Locate every Plasmodium falciparum-infected red blood cell.
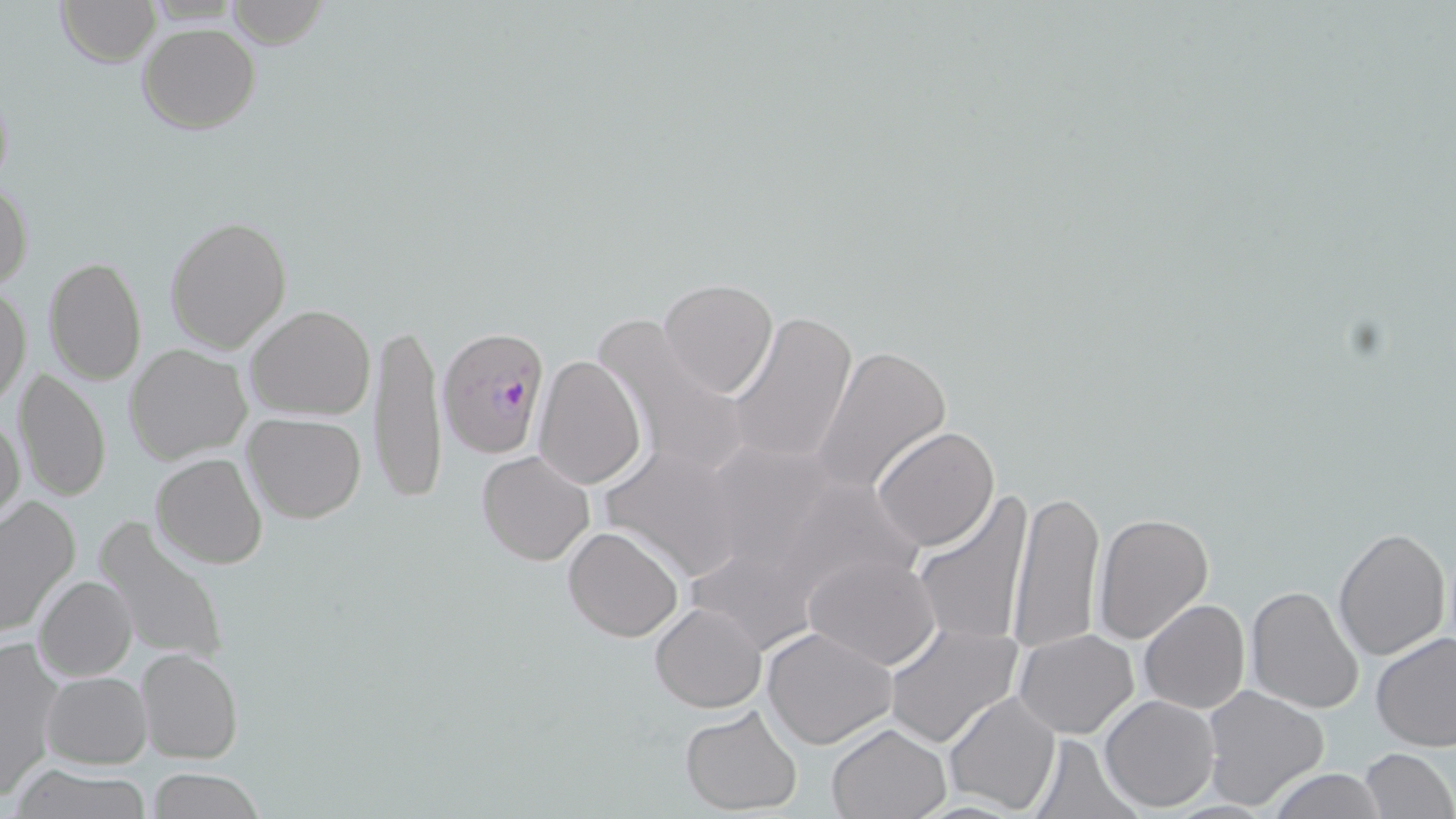
Approximate bounding boxes as (x1,y1)-(x2,y2) corner pairs in pixels.
Plasmodium falciparum-infected red blood cells: (439,327)-(552,457).

slide-level diagnosis = Plasmodium falciparum
image size = 1456×819 pixels
field of view = single
preparation = thin blood smear
magnification = 1000x
stain = May-Grünwald-Giemsa
modality = optical microscopy
uninfected red blood cell locations = approximate bounding boxes as (x1,y1)-(x2,y2) corner pairs in pixels: (55,0)-(159,67), (227,0)-(326,49), (136,23)-(261,134), (0,180)-(33,295), (165,215)-(292,354), (43,255)-(147,387), (658,279)-(779,400), (0,285)-(30,412), (246,304)-(375,421), (726,310)-(858,467), (593,313)-(750,482), (372,318)-(447,506), (124,343)-(252,464), (811,344)-(953,495), (532,355)-(647,489), (11,367)-(112,504), (0,410)-(25,529), (242,412)-(366,524), (872,426)-(1001,551), (598,443)-(747,584), (477,449)-(596,566), (151,452)-(268,570), (1008,485)-(1105,656), (0,493)-(81,635), (913,494)-(1036,645), (95,514)-(230,669), (1094,514)-(1214,643), (562,526)-(685,642), (1334,527)-(1451,660), (805,554)-(941,671), (34,575)-(136,681), (1245,586)-(1365,715), (1138,600)-(1250,714), (649,603)-(766,712), (885,622)-(1023,751), (762,626)-(897,749), (1014,629)-(1139,739), (1371,631)-(1456,751), (1,637)-(64,798), (135,646)-(243,764), (43,672)-(152,767), (1201,685)-(1329,811), (944,691)-(1062,816), (1100,694)-(1219,810), (679,705)-(802,814), (826,723)-(950,819), (1029,735)-(1140,818), (1359,748)-(1455,819), (11,765)-(153,819), (144,767)-(267,819), (1266,767)-(1388,819)